Locate platelets.
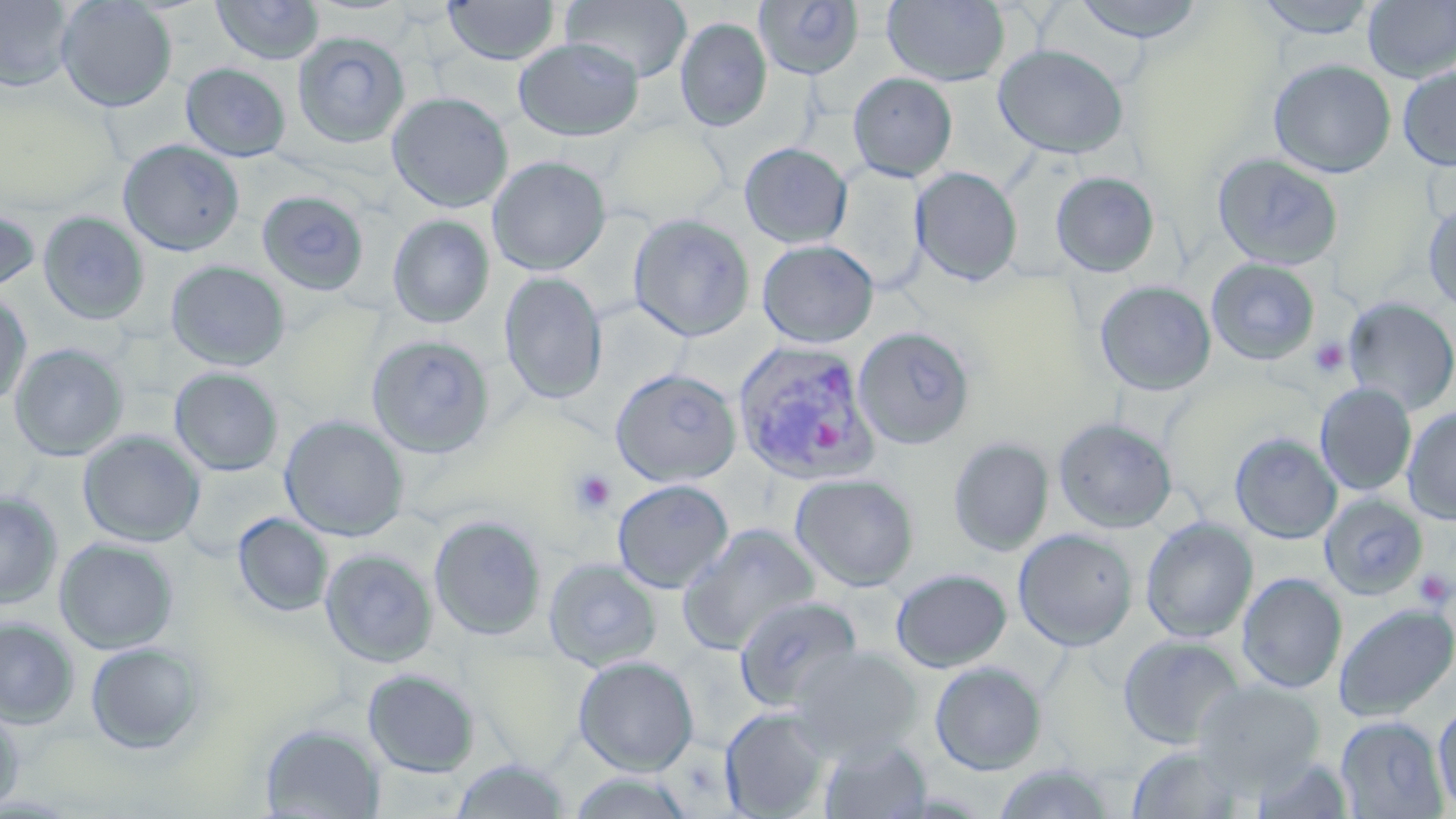
Approximate bounding boxes as (x1,y1)-(x2,y2) corner pairs in pixels.
Platelets: (1309,337)-(1350,378), (571,469)-(617,515), (1413,569)-(1454,608).

Plasmodium vivax-infected red blood cell locations: (731,341)-(882,487). Uninfected red blood cell locations: (0,0)-(76,92), (55,0)-(178,112), (211,0)-(324,65), (561,0)-(692,84), (882,0)-(1010,86), (1068,0)-(1210,44), (1253,0)-(1383,39), (442,1)-(561,65), (1363,1)-(1456,83), (755,2)-(864,80), (674,17)-(772,132), (292,31)-(410,148), (513,37)-(645,141), (993,43)-(1129,159), (1268,58)-(1396,178), (181,63)-(291,162), (1397,65)-(1456,172), (848,72)-(958,182), (386,91)-(513,213), (118,139)-(245,255), (739,142)-(852,248), (1211,152)-(1344,271), (487,156)-(611,275), (828,164)-(928,291), (911,167)-(1022,285), (1050,171)-(1160,277), (257,190)-(370,296), (1423,199)-(1456,312), (0,206)-(40,297), (38,211)-(150,326), (627,213)-(755,342), (387,214)-(496,327), (756,239)-(879,348), (1206,258)-(1320,365), (165,260)-(290,372), (499,272)-(608,404), (1094,280)-(1216,396), (0,290)-(32,410), (1342,296)-(1456,415), (853,327)-(975,450), (365,334)-(496,458), (9,343)-(128,461), (169,367)-(284,476), (610,368)-(742,487), (1315,383)-(1417,496), (1402,407)-(1456,524), (280,415)-(409,542), (1054,418)-(1177,533), (78,431)-(206,547), (1230,432)-(1342,544), (948,437)-(1054,556), (178,460)-(290,562), (790,473)-(919,591), (611,479)-(733,593), (0,491)-(63,608), (1318,493)-(1428,600), (232,512)-(333,617), (429,514)-(546,641), (1140,517)-(1258,643), (678,524)-(820,654), (1013,529)-(1138,651), (54,537)-(179,654), (320,548)-(438,667), (543,558)-(663,672), (553,561)-(685,763), (890,568)-(1012,672), (1237,573)-(1346,693), (1236,588)-(1455,702), (734,595)-(862,712), (1333,603)-(1456,722), (0,618)-(79,728), (1117,634)-(1246,750), (86,642)-(207,755), (789,645)-(921,759), (573,656)-(698,775), (929,661)-(1046,775), (362,668)-(480,777), (1194,680)-(1325,789), (1434,701)-(1456,814), (0,705)-(25,813), (720,706)-(831,818), (1335,716)-(1447,818), (258,723)-(386,819), (819,736)-(932,819), (1124,744)-(1251,819), (1250,754)-(1356,819), (448,757)-(573,818), (991,762)-(1117,818), (566,771)-(698,818). Slide-level diagnosis: Plasmodium vivax. May-Grünwald-Giemsa stain. 1000x magnification. Image is 1456×819 pixels. Single field of view. Light microscopy. Thin blood smear.